Outline each blood parasite and name the species.
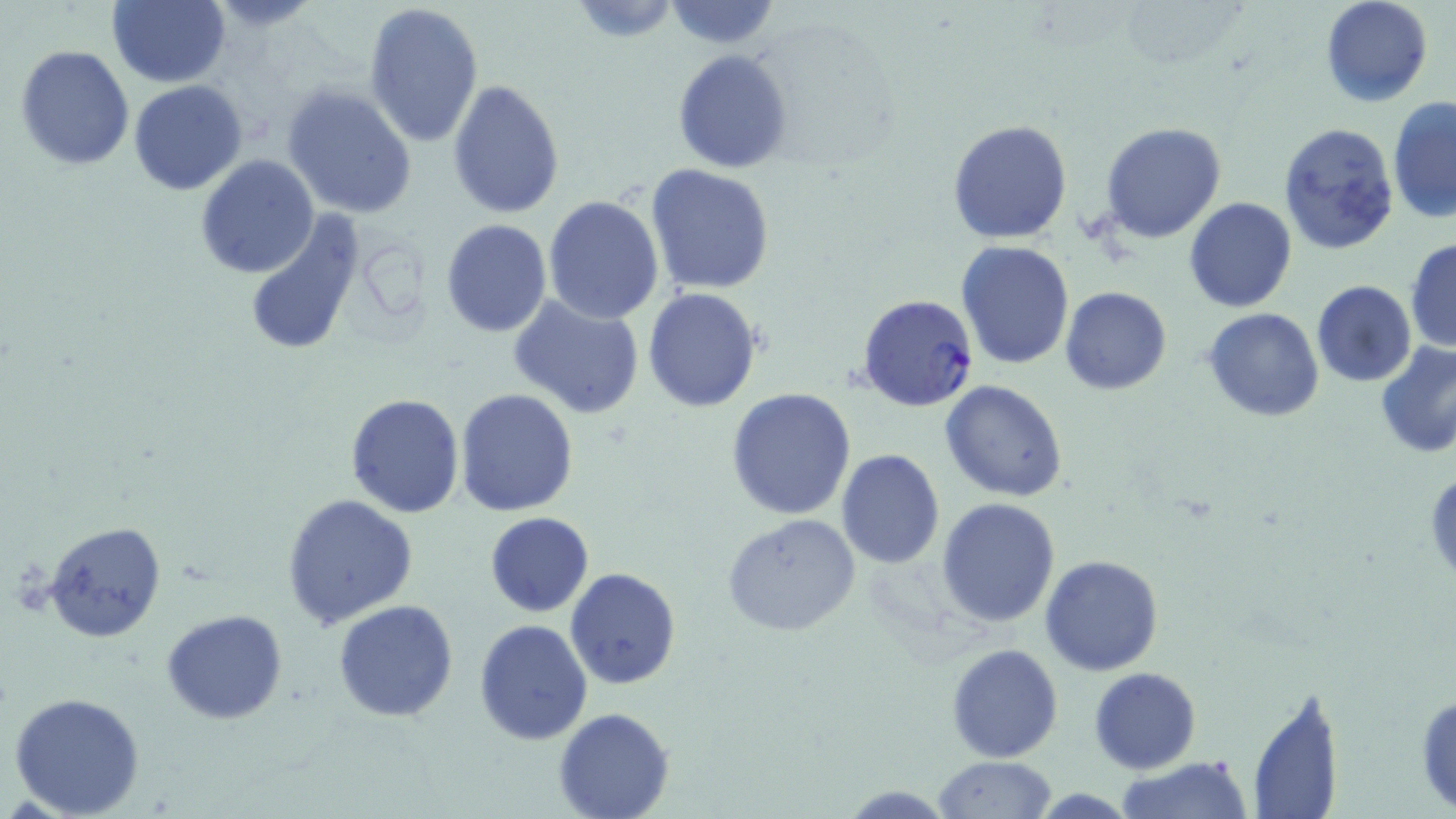

Approximate bounding boxes as (x1,y1)-(x2,y2) corner pairs in pixels.
Plasmodium falciparum-infected red blood cells: (855,292)-(980,412).
No Plasmodium ovale, Plasmodium malariae, Plasmodium vivax, Babesia divergens, or Trypanosoma brucei observed.

Summary:
  - Uninfected red blood cell locations: (1319,0)-(1433,106), (105,1)-(230,87), (566,1)-(685,42), (662,1)-(780,50), (364,2)-(485,150), (14,43)-(135,171), (672,48)-(794,173), (445,79)-(565,219), (129,80)-(248,196), (282,84)-(417,221), (1388,96)-(1456,224), (946,118)-(1072,243), (1276,122)-(1400,255), (1099,123)-(1226,243), (195,154)-(320,278), (645,162)-(775,294), (543,194)-(666,324), (1185,197)-(1297,312), (244,211)-(368,357), (441,220)-(552,337), (1405,236)-(1456,353), (955,241)-(1074,370), (1310,279)-(1417,386), (1060,287)-(1171,396), (642,288)-(762,412), (505,295)-(646,423), (1203,306)-(1324,422), (1373,341)-(1456,459), (941,379)-(1070,501), (455,387)-(580,516), (725,388)-(856,521), (345,391)-(466,519), (836,449)-(945,568), (1426,466)-(1456,585), (281,492)-(419,629), (936,497)-(1059,627), (484,512)-(594,616), (720,514)-(864,639), (43,521)-(165,644), (1040,555)-(1165,675), (565,567)-(681,690), (332,599)-(458,722), (161,609)-(289,726), (473,619)-(592,745), (946,643)-(1063,762), (1090,667)-(1201,774), (1244,687)-(1344,819), (1414,688)-(1456,816), (9,691)-(148,817), (552,708)-(674,819), (1116,755)-(1253,819), (933,756)-(1058,817), (838,784)-(958,817)
  - Slide-level diagnosis: Plasmodium falciparum
  - Modality: light microscopy
  - Magnification: 1000x
  - Field of view: single
  - Image size: 1456×819 pixels
  - Preparation: thin blood smear
  - Stain: May-Grünwald-Giemsa